Assess for malaria.
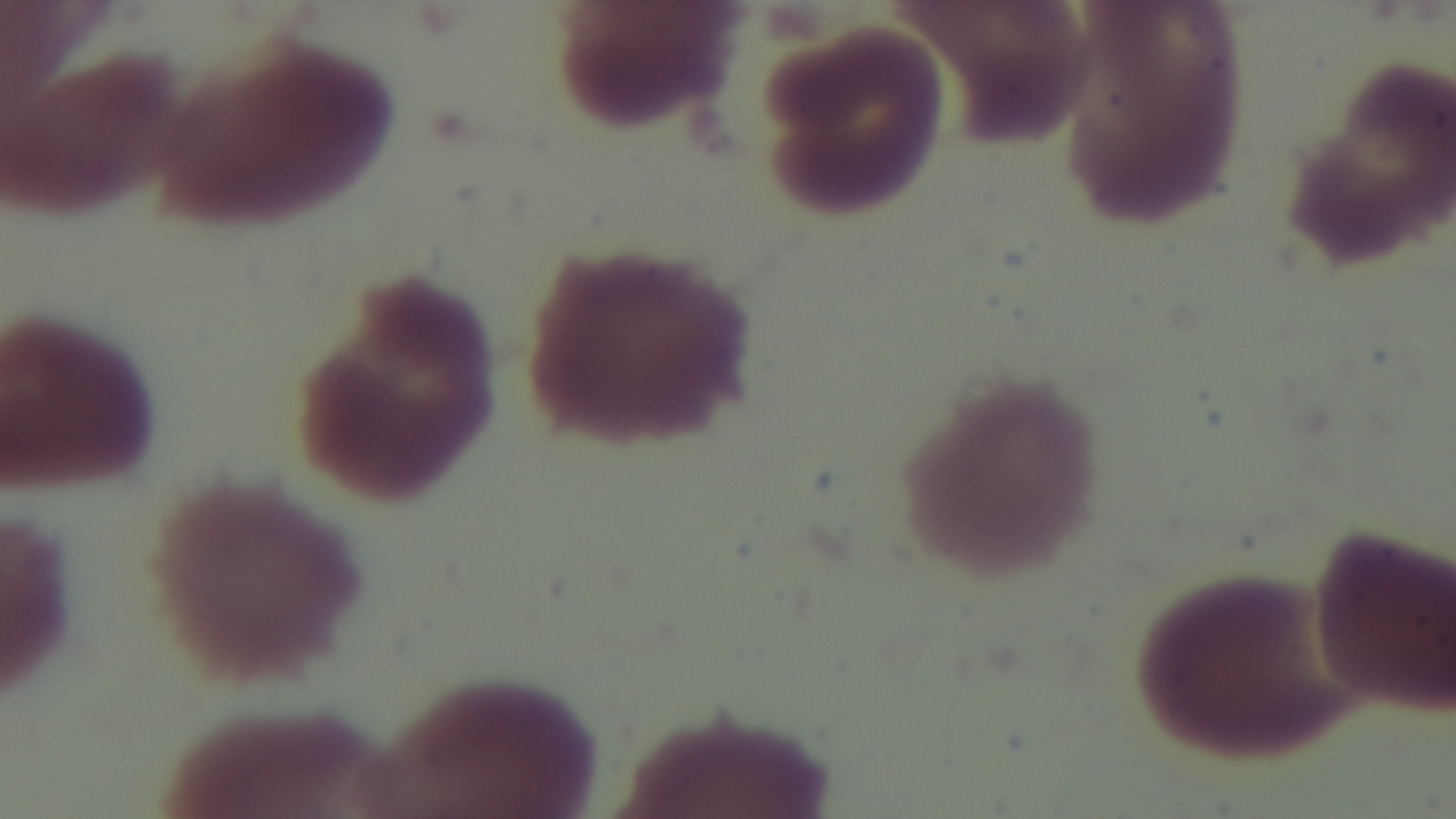

Uninfected.

One field from the slide. Preparation: thin blood film. Captured with a mounted 4K digital camera. Giemsa-stained. Photomicrograph. Oil-immersion objective, 100x.